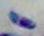 Photomicrograph. Toxoplasma gondii is seen. Captured at 1000x magnification.